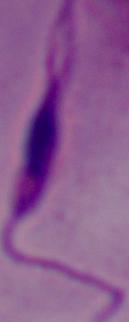 Captured at 1000x magnification. Micrograph. A Leishmania parasite is seen.